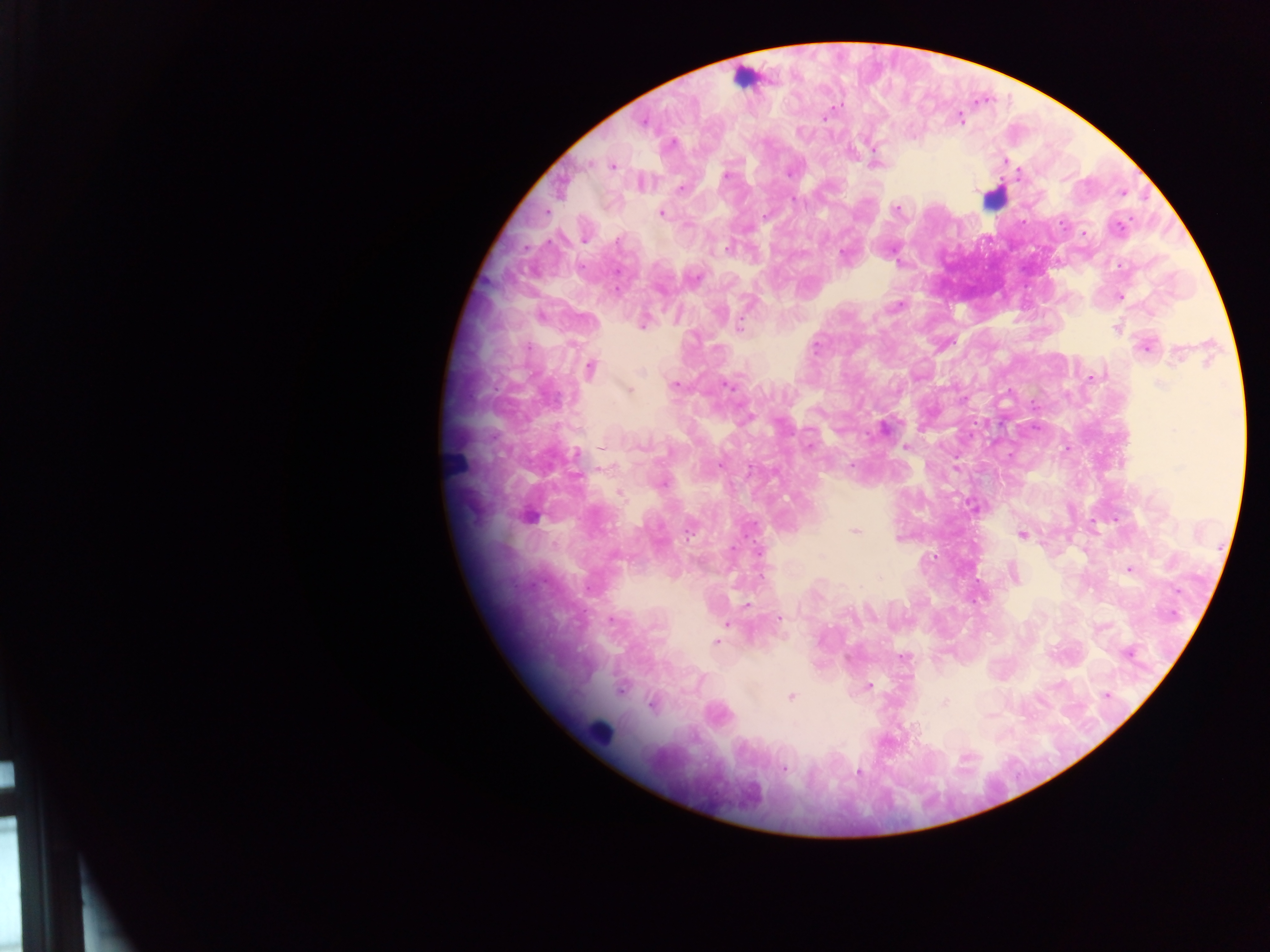
Approximate centers as x y in pixels. Malaria parasite locations: 824 118; 960 118; 643 121; 673 142; 1005 161; 613 166; 789 174; 726 175; 1020 175; 681 188; 793 200; 897 209; 662 214; 765 216; 1118 226; 1084 234; 618 242; 727 250; 843 255; 695 277; 1121 297; 898 306; 643 324; 739 325; 1116 329; 817 346; 1145 347; 1177 356; 591 368; 640 372; 1092 378; 1160 384; 676 385; 728 385; 630 390; 884 429; 1173 430; 809 445; 906 447; 602 448; 577 454; 719 466; 852 466; 748 468; 955 468; 663 484; 620 494; 972 506; 529 516; 854 531; 1022 535; 732 548; 1130 570; 589 589; 746 605; 1174 614; 779 618; 610 619; 727 624; 716 642; 1127 654; 903 658; 868 685; 1106 695; 791 696; 944 702; 652 704; 989 715; 784 769; 858 772. Leukocyte locations (subset; some below the resolvable size): 742 76; 993 198; 455 462; 598 731. Thick blood smear. Image is 1270×952 pixels. Collected in Ghana. Photographed through a microscope with a mobile-phone camera. Single field of view.